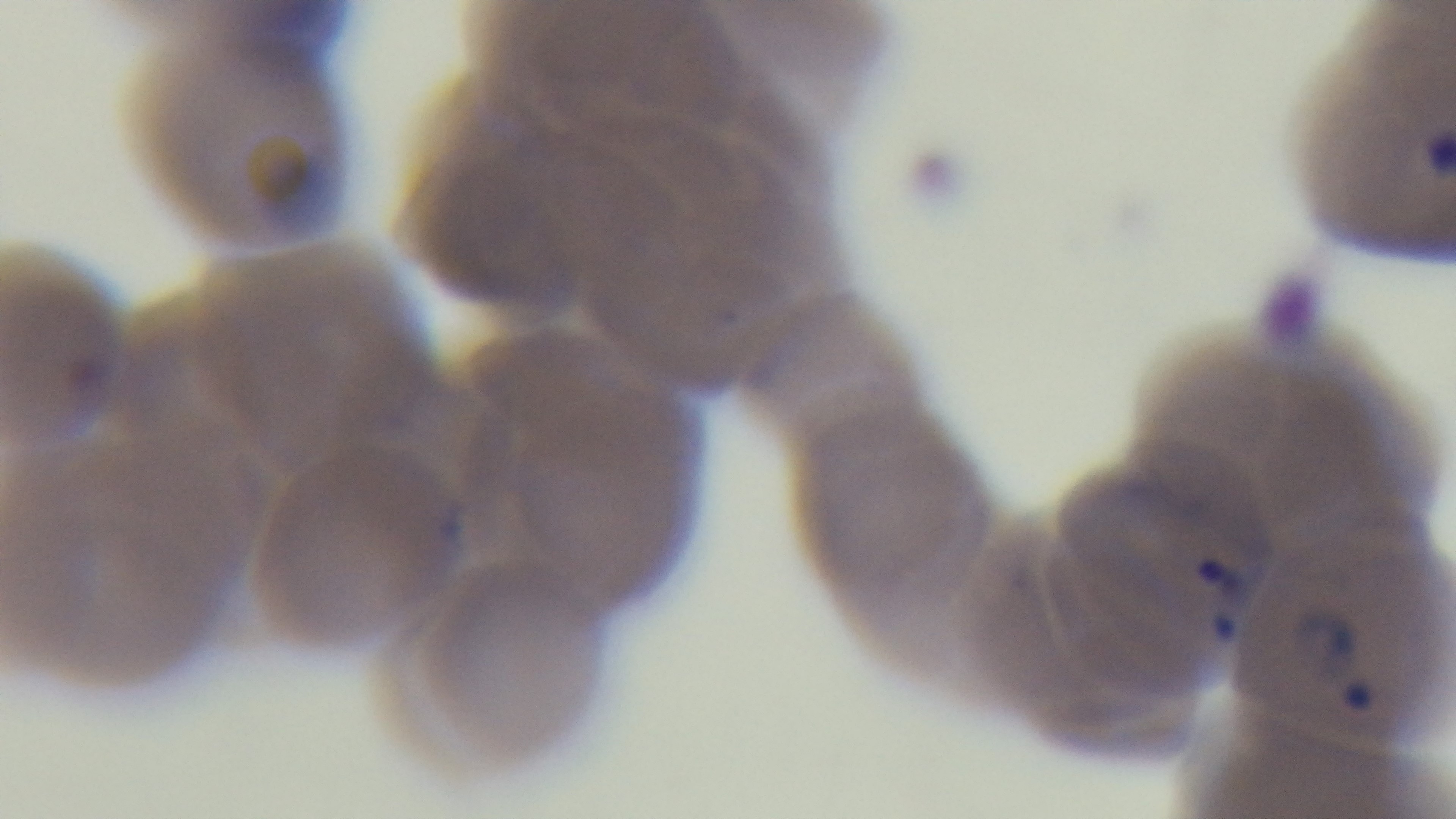
malaria status = positive
field of view = one from the slide
objective = 100x oil immersion
preparation = thin blood film
stain = Giemsa
capture = mounted 4K digital camera
modality = light microscopy